Name the parasite shown.
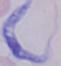

This is a trypanosome.

magnification = 1000x
modality = micrograph